Point out each Plasmodium parasite.
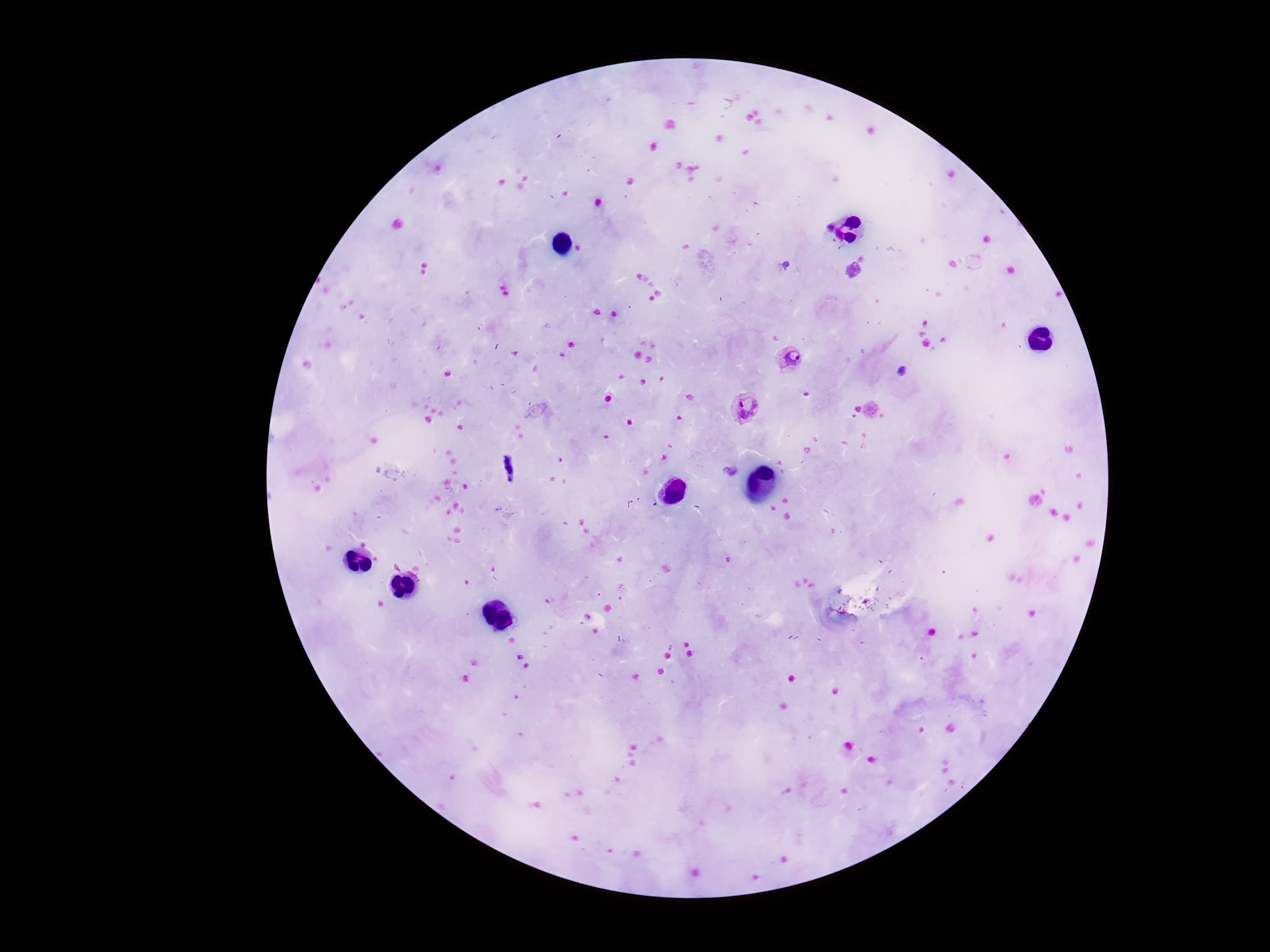

Approximate centers as (x, y) in pixels.
Plasmodium parasites: (789, 359), (747, 408).

Single field of view. Patient malaria status: infected. Photographed through the microscope eyepiece with a smartphone camera. Thick blood smear. Giemsa stain. Image is 1270×952 pixels. 100x magnification.